Comment on the morphology of the red blood cells.
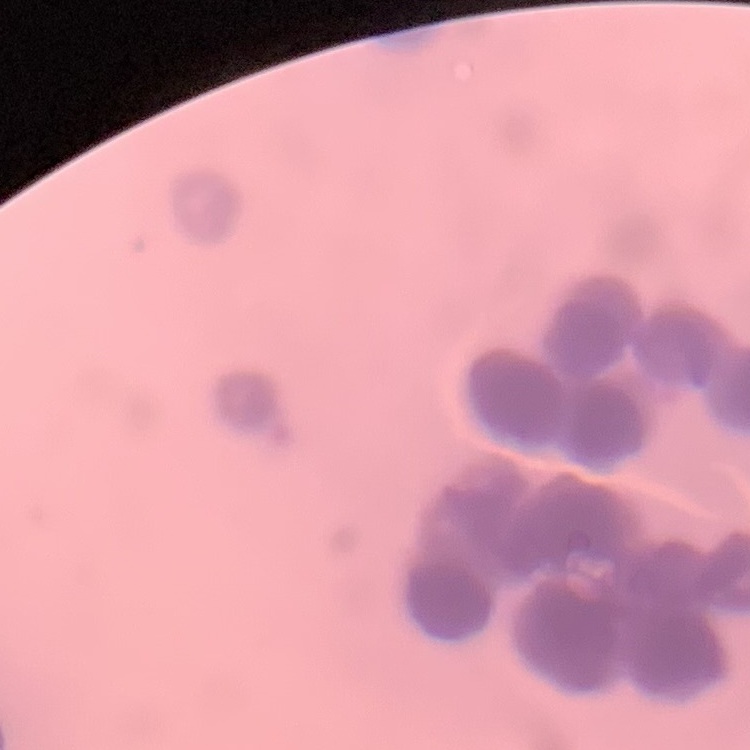

They show rouleaux formation.

Stained with either Field's or Giemsa. Thin blood smear. One tile cut from a larger photomicrograph.